Name the parasite shown.
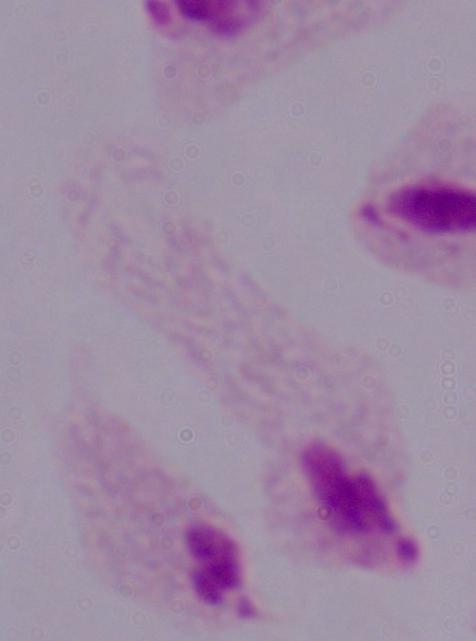

This is a trichomonad.

Micrograph. 1000x magnification.